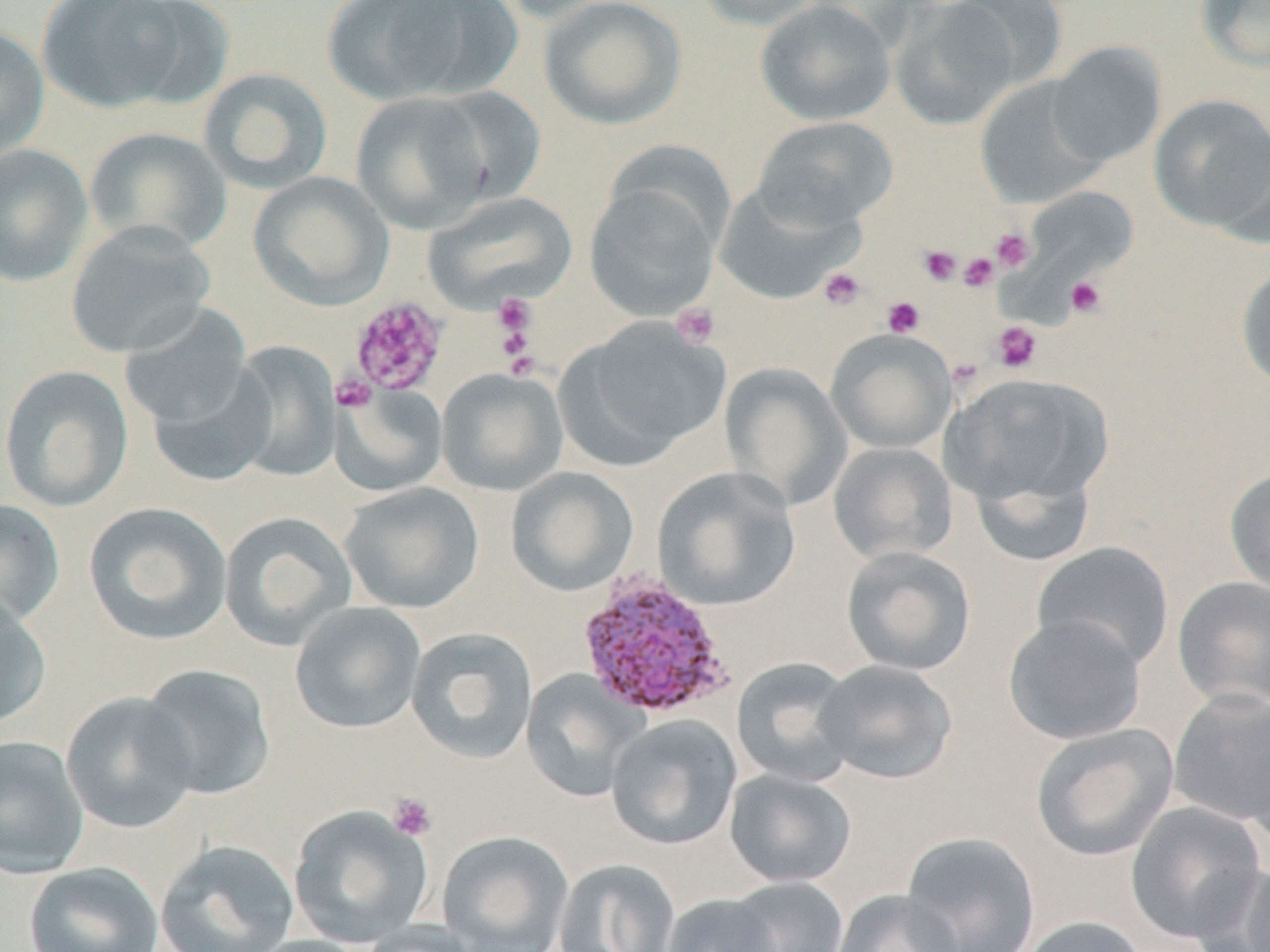

Plasmodium vivax-infected red blood cell locations = approximate bounding boxes as named x1/y1/x2/y2 corners in pixels: (x1=574, y1=570, x2=737, y2=721)
slide-level diagnosis = Plasmodium vivax
magnification = 1000x
uninfected red blood cell locations = approximate bounding boxes as named x1/y1/x2/y2 corners in pixels: (x1=35, y1=0, x2=199, y2=114), (x1=319, y1=0, x2=518, y2=105), (x1=492, y1=0, x2=625, y2=24), (x1=538, y1=0, x2=687, y2=130), (x1=689, y1=0, x2=830, y2=31), (x1=944, y1=0, x2=1070, y2=90), (x1=1195, y1=0, x2=1270, y2=73), (x1=754, y1=1, x2=895, y2=126), (x1=889, y1=2, x2=1020, y2=130), (x1=0, y1=23, x2=50, y2=161), (x1=1046, y1=41, x2=1166, y2=169), (x1=199, y1=67, x2=333, y2=194), (x1=974, y1=77, x2=1108, y2=209), (x1=424, y1=86, x2=546, y2=206), (x1=352, y1=91, x2=497, y2=233), (x1=1149, y1=93, x2=1270, y2=233), (x1=753, y1=115, x2=899, y2=229), (x1=85, y1=126, x2=231, y2=255), (x1=0, y1=144, x2=93, y2=287), (x1=248, y1=171, x2=394, y2=311), (x1=583, y1=172, x2=725, y2=323), (x1=713, y1=181, x2=861, y2=305), (x1=1024, y1=184, x2=1138, y2=284), (x1=424, y1=191, x2=577, y2=312), (x1=65, y1=221, x2=215, y2=359), (x1=1235, y1=263, x2=1270, y2=394), (x1=118, y1=305, x2=253, y2=429), (x1=557, y1=318, x2=728, y2=469), (x1=827, y1=329, x2=956, y2=454), (x1=227, y1=341, x2=341, y2=482), (x1=720, y1=363, x2=852, y2=509), (x1=0, y1=364, x2=134, y2=512), (x1=147, y1=364, x2=277, y2=488), (x1=436, y1=368, x2=569, y2=496), (x1=941, y1=371, x2=1112, y2=514), (x1=330, y1=384, x2=448, y2=496), (x1=827, y1=442, x2=957, y2=565), (x1=1224, y1=465, x2=1270, y2=599), (x1=506, y1=466, x2=639, y2=596), (x1=652, y1=467, x2=801, y2=612), (x1=340, y1=482, x2=485, y2=614), (x1=0, y1=498, x2=66, y2=630), (x1=83, y1=501, x2=232, y2=646), (x1=219, y1=511, x2=358, y2=650), (x1=1031, y1=541, x2=1175, y2=672), (x1=841, y1=545, x2=976, y2=677), (x1=1172, y1=576, x2=1270, y2=710), (x1=0, y1=596, x2=51, y2=730), (x1=289, y1=602, x2=427, y2=734), (x1=1002, y1=613, x2=1147, y2=745), (x1=406, y1=626, x2=538, y2=764), (x1=730, y1=656, x2=861, y2=786), (x1=815, y1=659, x2=959, y2=785), (x1=136, y1=663, x2=275, y2=801), (x1=521, y1=669, x2=645, y2=802), (x1=1168, y1=690, x2=1270, y2=828), (x1=61, y1=692, x2=198, y2=834), (x1=606, y1=714, x2=742, y2=850), (x1=1030, y1=724, x2=1178, y2=862), (x1=0, y1=735, x2=89, y2=878), (x1=725, y1=769, x2=857, y2=888), (x1=1124, y1=800, x2=1266, y2=943), (x1=288, y1=805, x2=433, y2=949), (x1=437, y1=831, x2=574, y2=952), (x1=901, y1=831, x2=1041, y2=952), (x1=155, y1=839, x2=299, y2=952), (x1=553, y1=858, x2=681, y2=952), (x1=1192, y1=861, x2=1270, y2=952), (x1=23, y1=862, x2=163, y2=952), (x1=719, y1=876, x2=848, y2=952), (x1=832, y1=889, x2=964, y2=952), (x1=660, y1=893, x2=783, y2=952), (x1=1016, y1=915, x2=1149, y2=952), (x1=359, y1=921, x2=483, y2=952), (x1=242, y1=935, x2=376, y2=952)
modality = optical microscopy
stain = May-Grünwald-Giemsa
platelet locations = approximate bounding boxes as named x1/y1/x2/y2 corners in pixels: (x1=990, y1=227, x2=1035, y2=272), (x1=918, y1=245, x2=961, y2=285), (x1=958, y1=252, x2=998, y2=291), (x1=817, y1=267, x2=867, y2=311), (x1=1065, y1=276, x2=1107, y2=318), (x1=492, y1=292, x2=537, y2=345), (x1=347, y1=295, x2=448, y2=397), (x1=882, y1=296, x2=926, y2=337), (x1=671, y1=302, x2=722, y2=349), (x1=991, y1=321, x2=1042, y2=373), (x1=948, y1=358, x2=984, y2=391), (x1=332, y1=374, x2=377, y2=412), (x1=387, y1=793, x2=437, y2=841)
preparation = thin blood film
field of view = one of a larger specimen
image size = 1270×952 pixels